Identify the parasite.
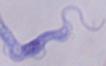
This is a trypanosome.

magnification = 1000x
modality = micrograph